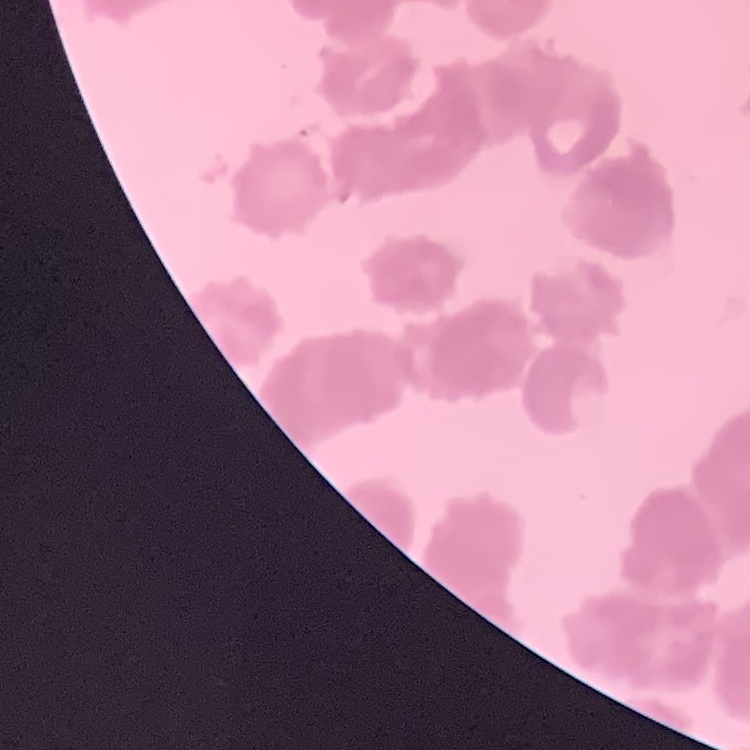

Summary:
  - Red blood cell morphology: rouleaux formation
  - Preparation: thin peripheral smear
  - Image type: one tile cut from a larger photomicrograph
  - Stain: Field's or Giemsa